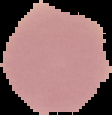

Summary:
  - Result: no Plasmodium parasites seen
  - Image size: 112×115 pixels
  - Preparation: thin blood smear
  - Image type: cell region segmented out of the field of view; surrounding area masked to black